Locate every Plasmodium ovale-infected red blood cell.
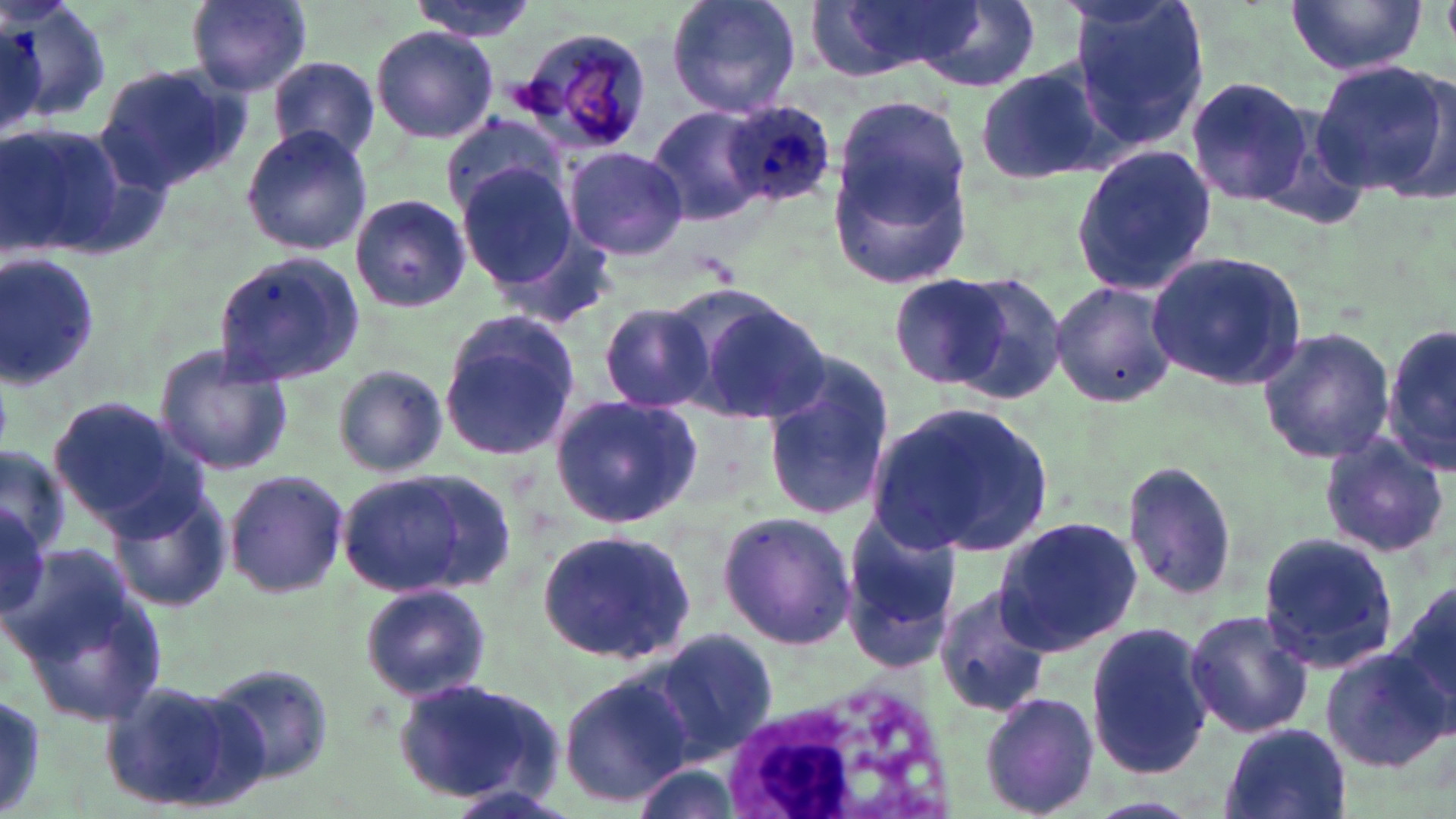
Approximate bounding boxes as named x1/y1/x2/y2 corners in pixels.
Plasmodium ovale-infected red blood cells: (x1=719, y1=102, x2=836, y2=210).

Summary:
  - Uninfected red blood cell locations: (x1=6, y1=0, x2=111, y2=129), (x1=186, y1=0, x2=311, y2=95), (x1=406, y1=0, x2=537, y2=40), (x1=663, y1=0, x2=803, y2=120), (x1=811, y1=0, x2=981, y2=81), (x1=1067, y1=0, x2=1211, y2=153), (x1=1283, y1=0, x2=1427, y2=77), (x1=910, y1=4, x2=1039, y2=92), (x1=510, y1=22, x2=652, y2=154), (x1=370, y1=25, x2=499, y2=142), (x1=266, y1=55, x2=379, y2=163), (x1=1308, y1=58, x2=1456, y2=202), (x1=973, y1=61, x2=1115, y2=187), (x1=94, y1=62, x2=247, y2=197), (x1=1186, y1=77, x2=1318, y2=209), (x1=835, y1=98, x2=975, y2=235), (x1=646, y1=105, x2=767, y2=227), (x1=439, y1=112, x2=573, y2=223), (x1=2, y1=122, x2=125, y2=259), (x1=240, y1=126, x2=373, y2=256), (x1=1070, y1=144, x2=1216, y2=296), (x1=564, y1=146, x2=689, y2=262), (x1=830, y1=151, x2=977, y2=288), (x1=457, y1=162, x2=581, y2=290), (x1=348, y1=195, x2=471, y2=313), (x1=0, y1=247, x2=103, y2=393), (x1=210, y1=250, x2=367, y2=389), (x1=1145, y1=251, x2=1309, y2=392), (x1=946, y1=272, x2=1067, y2=403), (x1=891, y1=274, x2=1011, y2=387), (x1=1049, y1=282, x2=1180, y2=409), (x1=683, y1=295, x2=831, y2=424), (x1=599, y1=302, x2=715, y2=416), (x1=437, y1=310, x2=585, y2=462), (x1=1385, y1=319, x2=1456, y2=479), (x1=1256, y1=326, x2=1395, y2=466), (x1=153, y1=348, x2=297, y2=475), (x1=764, y1=361, x2=897, y2=525), (x1=332, y1=364, x2=448, y2=478), (x1=549, y1=393, x2=701, y2=529), (x1=47, y1=397, x2=205, y2=530), (x1=867, y1=402, x2=1054, y2=561), (x1=1318, y1=432, x2=1451, y2=561), (x1=1, y1=444, x2=70, y2=556), (x1=1121, y1=461, x2=1241, y2=603), (x1=222, y1=467, x2=348, y2=601), (x1=338, y1=467, x2=513, y2=602), (x1=105, y1=480, x2=235, y2=614), (x1=0, y1=499, x2=58, y2=633), (x1=717, y1=511, x2=856, y2=651), (x1=840, y1=516, x2=961, y2=673), (x1=993, y1=517, x2=1142, y2=653), (x1=535, y1=527, x2=698, y2=665), (x1=1259, y1=530, x2=1397, y2=677), (x1=12, y1=562, x2=171, y2=726), (x1=1392, y1=575, x2=1456, y2=724), (x1=360, y1=583, x2=492, y2=701), (x1=934, y1=585, x2=1054, y2=717), (x1=1184, y1=609, x2=1314, y2=738), (x1=1086, y1=623, x2=1213, y2=780), (x1=652, y1=629, x2=778, y2=759), (x1=1320, y1=645, x2=1453, y2=772), (x1=206, y1=661, x2=337, y2=789), (x1=558, y1=673, x2=692, y2=806), (x1=102, y1=677, x2=265, y2=812), (x1=391, y1=677, x2=564, y2=807), (x1=0, y1=687, x2=50, y2=819), (x1=978, y1=690, x2=1101, y2=819), (x1=1217, y1=722, x2=1351, y2=819), (x1=627, y1=763, x2=743, y2=819)
  - White blood cell locations: (x1=713, y1=680, x2=963, y2=819)
  - Slide-level diagnosis: Plasmodium ovale
  - Magnification: 1000x
  - Field of view: one of a larger specimen
  - Stain: May-Grünwald-Giemsa
  - Image size: 1456×819 pixels
  - Preparation: thin blood smear
  - Modality: optical microscopy